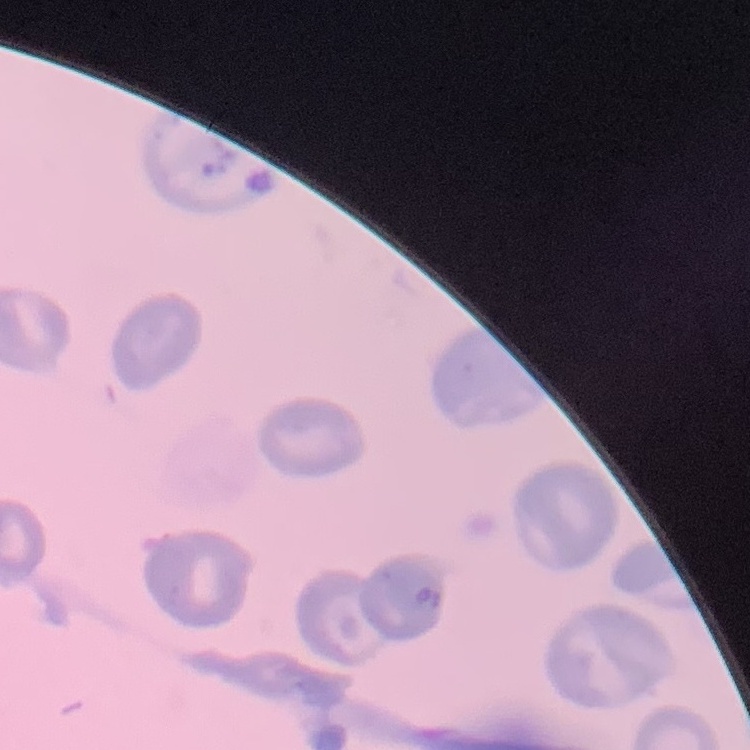
The erythrocytes exhibit no rouleaux formation. Stained with either Field's or Giemsa. One tile cut from a larger photomicrograph. Thin blood film.